Classify this cell by malaria status.
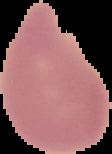
It is uninfected.

{
  "preparation": "thin blood smear",
  "image_type": "segmented cell region on a black background",
  "image_size": "112×154 pixels"
}